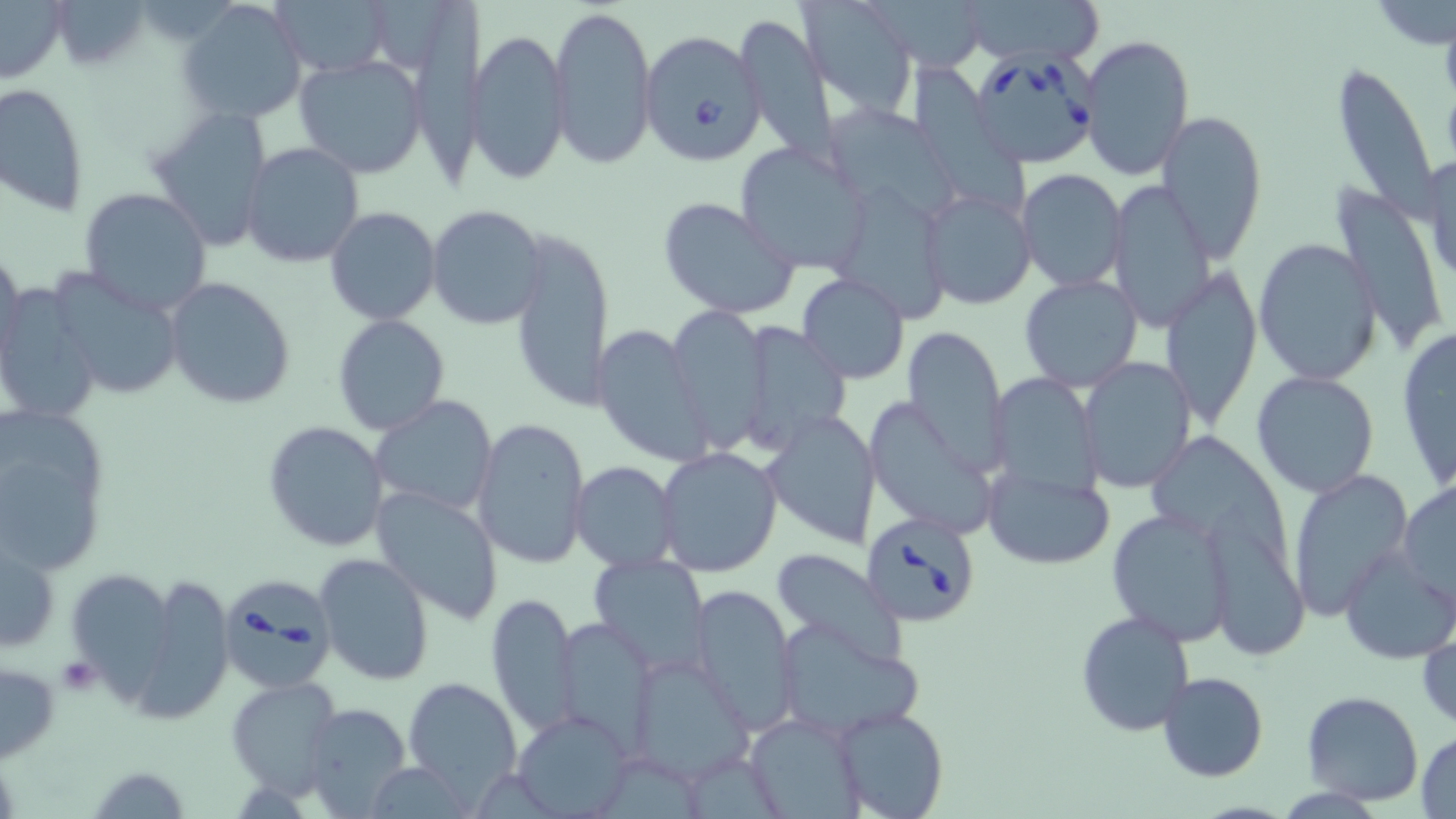
Summary:
  - Coordinate format: approximate bounding boxes as (x1,y1)-(x2,y2) corner pairs in pixels
  - Uninfected red blood cell locations: (47,0)-(154,68), (797,0)-(918,111), (875,0)-(989,70), (973,0)-(1099,67), (1376,0)-(1455,50), (179,1)-(308,126), (275,1)-(391,78), (421,1)-(493,193), (0,2)-(67,84), (550,3)-(657,169), (735,16)-(839,167), (469,30)-(569,187), (1081,32)-(1195,181), (293,55)-(426,177), (1331,62)-(1443,221), (912,65)-(1027,217), (0,82)-(90,218), (144,105)-(273,252), (1157,108)-(1268,261), (837,113)-(957,227), (735,142)-(874,275), (240,143)-(365,267), (1419,153)-(1456,288), (1016,167)-(1127,292), (1108,180)-(1215,331), (841,186)-(945,326), (1328,186)-(1448,356), (78,188)-(215,318), (919,191)-(1037,310), (657,196)-(804,321), (426,204)-(548,331), (325,206)-(441,325), (507,225)-(614,413), (1253,238)-(1383,386), (0,247)-(24,375), (45,265)-(187,402), (1161,267)-(1259,431), (797,273)-(910,383), (163,275)-(296,409), (1018,275)-(1142,392), (0,282)-(104,422), (668,307)-(771,451), (333,314)-(451,437), (734,321)-(850,454), (593,323)-(714,468), (903,325)-(1007,478), (1394,328)-(1456,492), (1078,357)-(1196,492), (1251,370)-(1381,499), (986,373)-(1105,504), (370,395)-(497,518), (865,397)-(1001,540), (0,401)-(113,575), (762,409)-(881,550), (474,417)-(591,569), (261,421)-(387,553), (655,446)-(782,574), (570,461)-(681,570), (984,466)-(1113,567), (1287,471)-(1414,623), (1398,479)-(1456,607), (370,487)-(503,625), (1106,507)-(1238,646), (1200,512)-(1312,661), (1,533)-(60,655), (1338,544)-(1455,665), (769,547)-(909,668), (315,552)-(434,684), (589,553)-(710,671), (123,573)-(234,727), (689,583)-(800,733), (486,593)-(578,738), (1075,609)-(1195,736), (555,616)-(659,753), (773,618)-(922,741), (1417,624)-(1455,733), (629,653)-(753,782), (0,659)-(60,764), (1158,670)-(1269,782), (402,675)-(524,802), (226,676)-(343,800), (1302,691)-(1425,805), (301,703)-(412,817), (833,706)-(951,819), (515,710)-(632,816), (746,712)-(866,818), (1414,731)-(1456,817)
  - Babesia divergens-infected red blood cell locations: (638,28)-(767,165), (974,50)-(1098,169), (859,513)-(981,626), (218,572)-(337,692)
  - Platelet locations: (56,658)-(102,696)
  - Slide-level diagnosis: Babesia divergens
  - Magnification: 1000x
  - Preparation: thin blood smear
  - Field of view: one of a larger specimen
  - Stain: May-Grünwald-Giemsa
  - Image size: 1456×819 pixels
  - Modality: optical microscopy